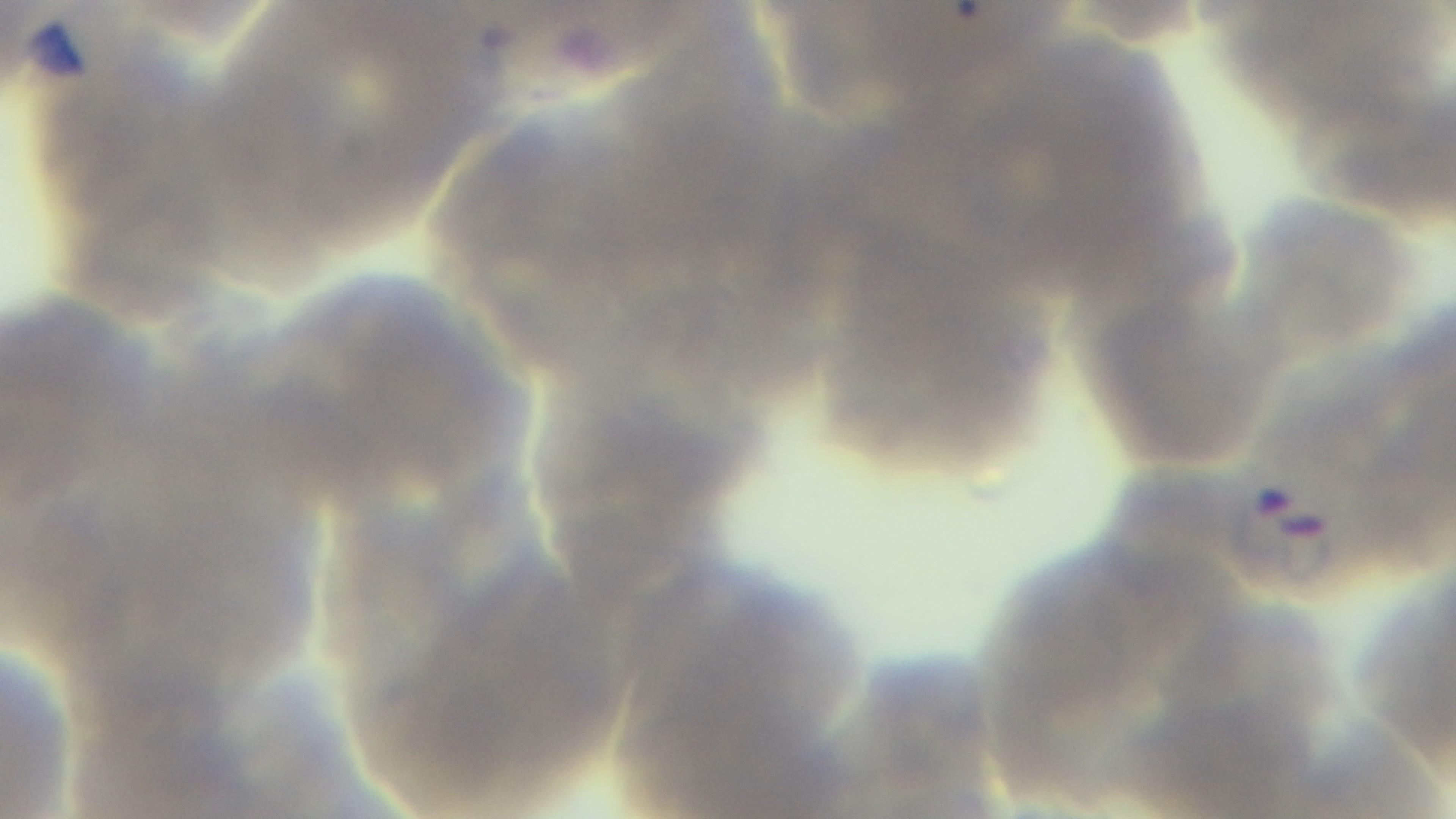 Captured with a mounted 4K digital camera. Preparation: thin smear. Malaria status: infected. 100x oil-immersion objective. Single field of view. Photomicrograph. Giemsa-stained.